Classify this cell by malaria status.
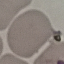
Uninfected.

capture = smartphone through the microscope eyepiece
preparation = thin blood smear
stain = Giemsa
image type = automatically extracted cell patch, resized to 64 × 64 pixels